Name the parasite shown.
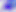

This is Toxoplasma gondii.

Photomicrograph. 400x magnification.